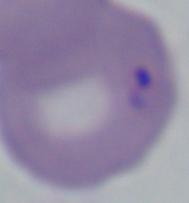
A Babesia parasite is shown. Photomicrograph. Captured at 1000x magnification.